Comment on the morphology of the erythrocytes.
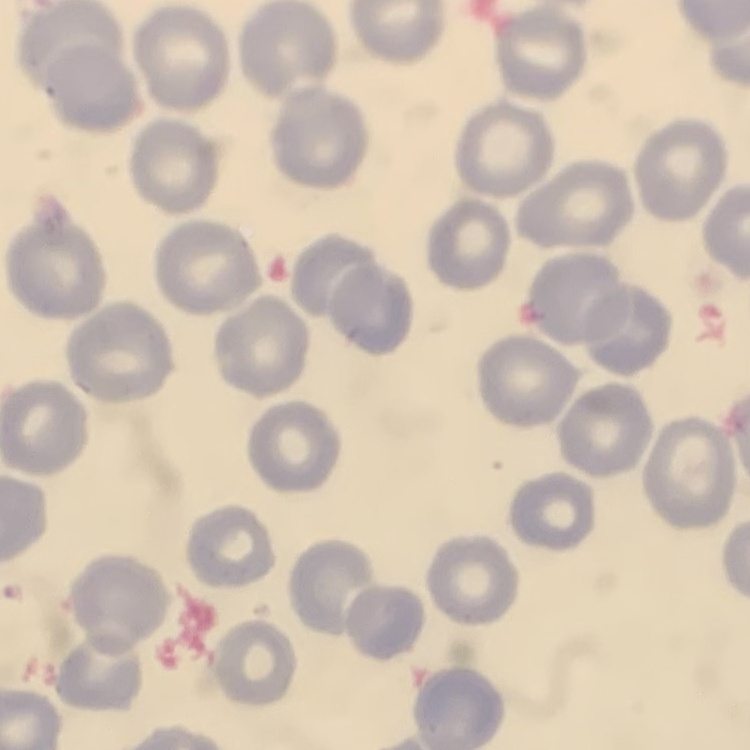

No rouleaux formation.

Thin blood film. Field's or Giemsa stain. One tile cut from a larger photomicrograph.